Name the parasite shown.
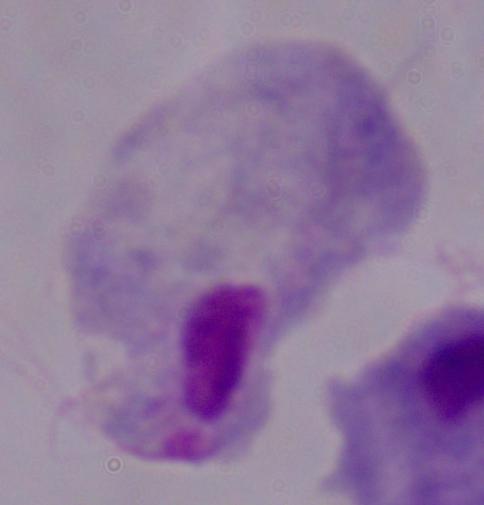

A trichomonad.

Summary:
  - Modality: micrograph
  - Magnification: 1000x